Classify the preparation.
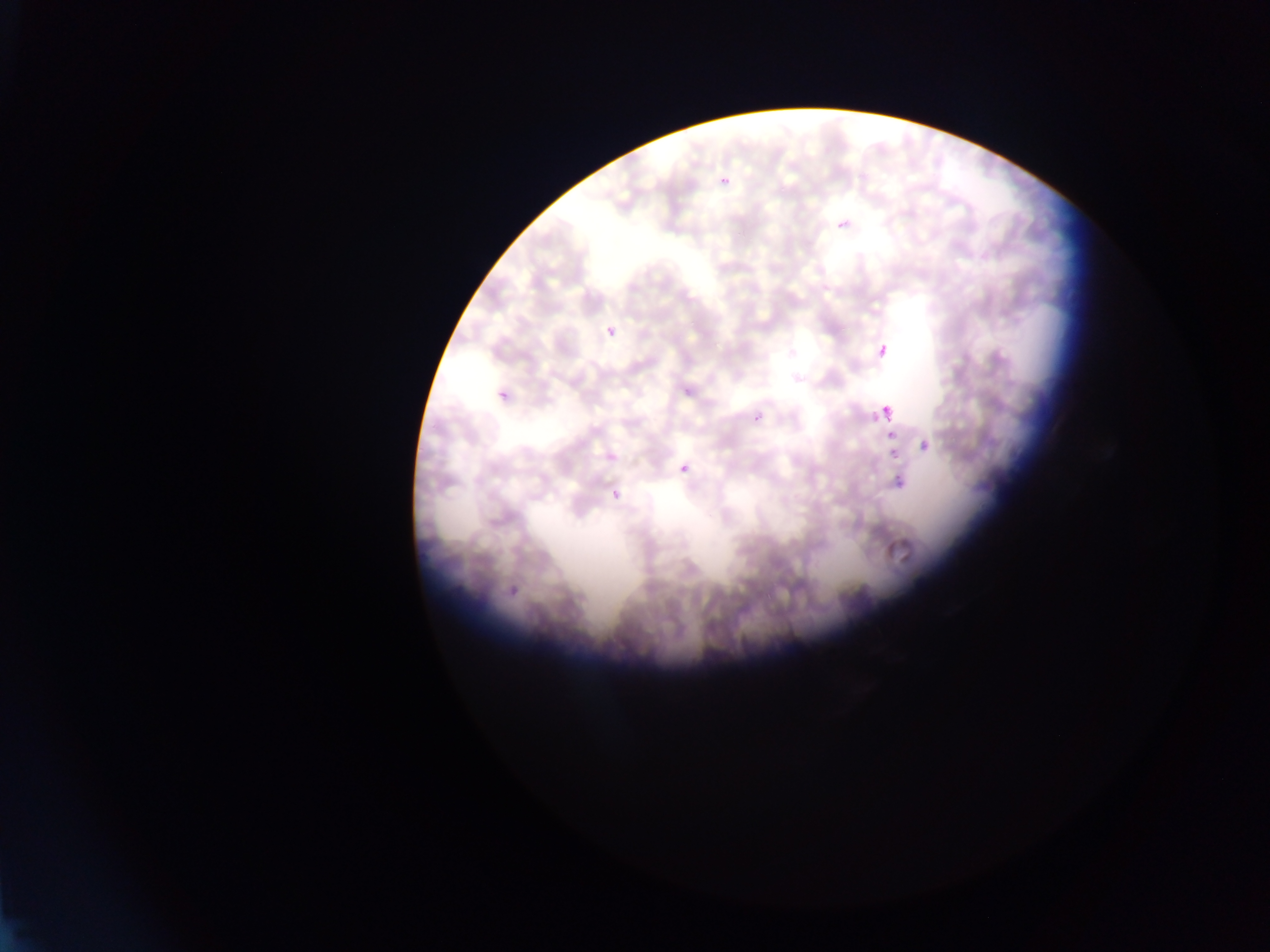
Thin blood smear.

artifact_stain_precipitate_or_debris_locations: 'approximate bounding boxes as left top right bottom in pixels: 881 400 892 422'
field_of_view: single
image_size: 1270×952 pixels
country: Ghana
capture: mobile-phone photograph through a microscope